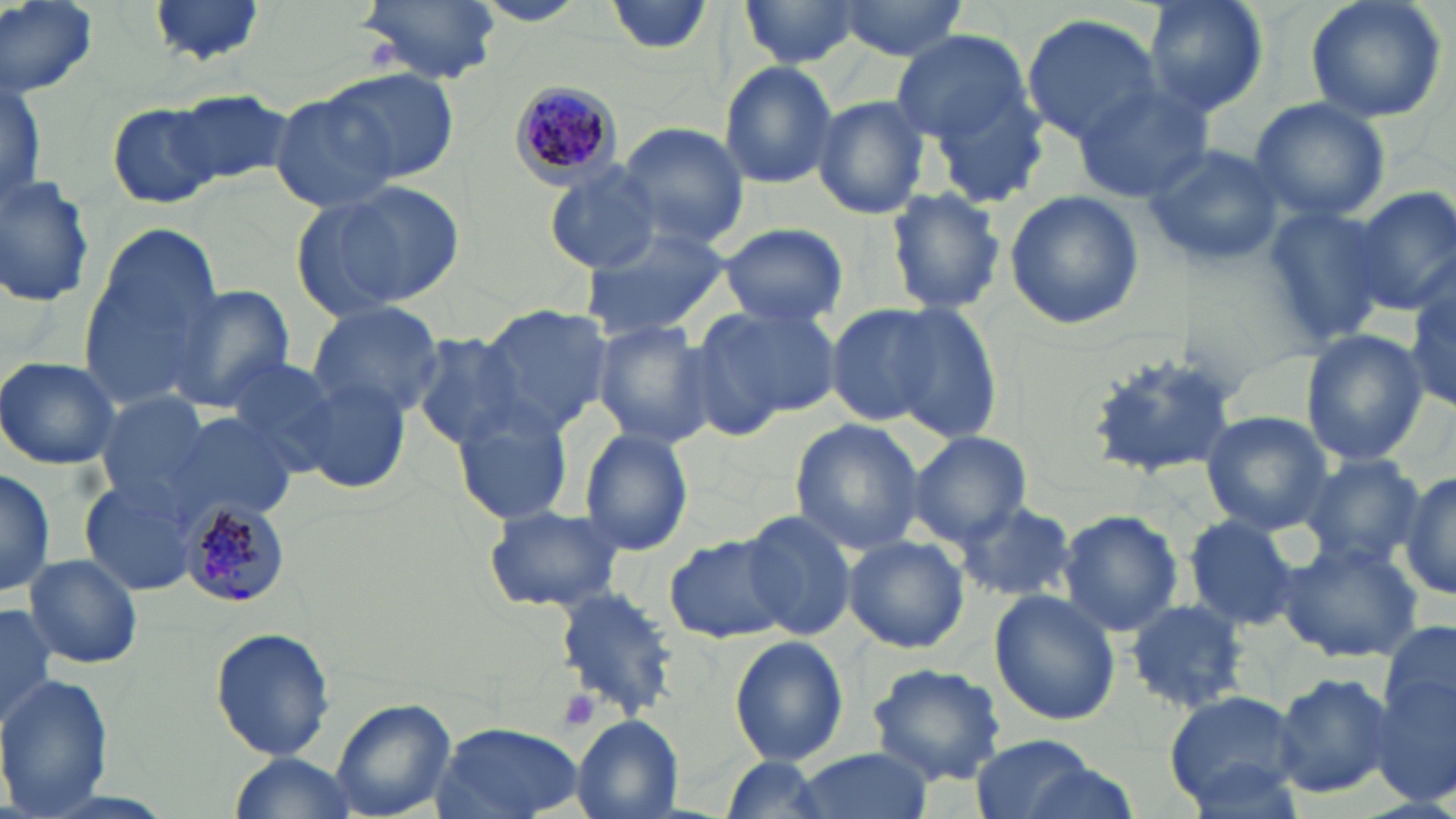
Approximate bounding boxes as (x1, y1, x2, y2) in pixels. Plasmodium malariae-infected red blood cell locations: (512, 83, 618, 190), (178, 499, 288, 607). Platelet locations: (556, 686, 602, 732). Uninfected red blood cell locations: (1, 0, 101, 98), (147, 0, 268, 70), (358, 0, 504, 85), (606, 0, 717, 55), (833, 0, 970, 61), (1141, 0, 1269, 115), (1304, 0, 1448, 125), (735, 1, 865, 71), (1020, 14, 1163, 146), (890, 32, 1033, 147), (718, 61, 840, 189), (917, 65, 1054, 208), (321, 67, 460, 187), (1071, 82, 1214, 203), (170, 88, 293, 189), (269, 91, 405, 214), (810, 93, 930, 220), (1247, 96, 1392, 222), (109, 103, 222, 209), (615, 122, 749, 248), (1140, 143, 1288, 267), (543, 163, 664, 273), (0, 171, 96, 310), (293, 180, 464, 318), (883, 187, 1008, 315), (1348, 187, 1456, 318), (1003, 190, 1143, 329), (1261, 206, 1391, 342), (717, 222, 848, 327), (580, 224, 734, 338), (77, 225, 223, 404), (1407, 280, 1456, 416), (166, 286, 294, 410), (691, 299, 844, 429), (305, 301, 446, 421), (472, 303, 610, 434), (824, 304, 948, 429), (888, 305, 1006, 441), (590, 319, 716, 446), (1300, 330, 1428, 466), (411, 334, 527, 448), (1087, 343, 1249, 478), (0, 355, 124, 470), (217, 356, 342, 477), (290, 375, 414, 496), (92, 391, 217, 507), (451, 405, 577, 527), (1199, 411, 1333, 534), (164, 413, 300, 526), (788, 418, 925, 554), (579, 427, 693, 556), (908, 432, 1033, 545), (1299, 455, 1426, 571), (0, 466, 55, 601), (1397, 471, 1456, 600), (79, 477, 205, 595), (955, 500, 1078, 604), (483, 504, 625, 612), (1056, 509, 1183, 637), (741, 510, 861, 639), (1185, 515, 1302, 630), (842, 534, 970, 654), (663, 536, 791, 646), (1280, 540, 1424, 662), (24, 554, 143, 671), (553, 586, 679, 718), (989, 591, 1121, 726), (1125, 598, 1251, 712), (0, 604, 58, 734), (1381, 614, 1456, 747), (209, 626, 337, 762), (731, 636, 848, 764), (867, 663, 1008, 787), (1272, 671, 1396, 797), (1371, 671, 1456, 812), (0, 672, 114, 819), (1163, 690, 1308, 813), (330, 697, 457, 817), (570, 714, 684, 818), (433, 723, 587, 818), (970, 732, 1104, 819), (791, 748, 934, 819), (226, 754, 360, 818), (720, 756, 831, 819). Slide-level diagnosis: Plasmodium malariae. One field of a larger specimen. May-Grünwald-Giemsa stain. Captured at 1000x magnification. Image is 1456×819 pixels. Thin blood film. Optical microscopy.